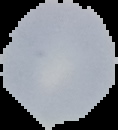
image type = segmented cell region on a black background
preparation = thin blood smear
result = no Plasmodium parasites detected
image size = 118×130 pixels